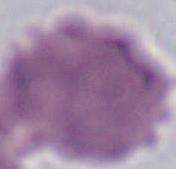
Micrograph. A red blood cell is shown. Captured at 1000x magnification.